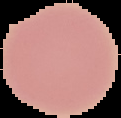

Image is 121×118 pixels. From a thin blood film. Malaria status: uninfected. Segmented cell region on a black background.